Identify the parasite.
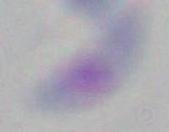

Toxoplasma gondii.

Micrograph. Captured at 1000x magnification.